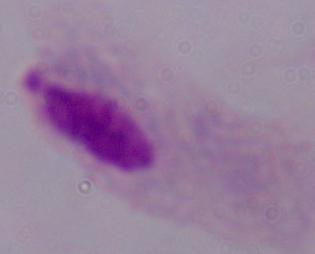

Summary:
  - Modality: photomicrograph
  - Identification: trichomonad
  - Magnification: 1000x